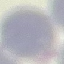

malaria status = uninfected
preparation = thin blood smear
stain = Giemsa
image type = automatically extracted cell patch, resized to 64 × 64 pixels
capture = smartphone through the microscope eyepiece